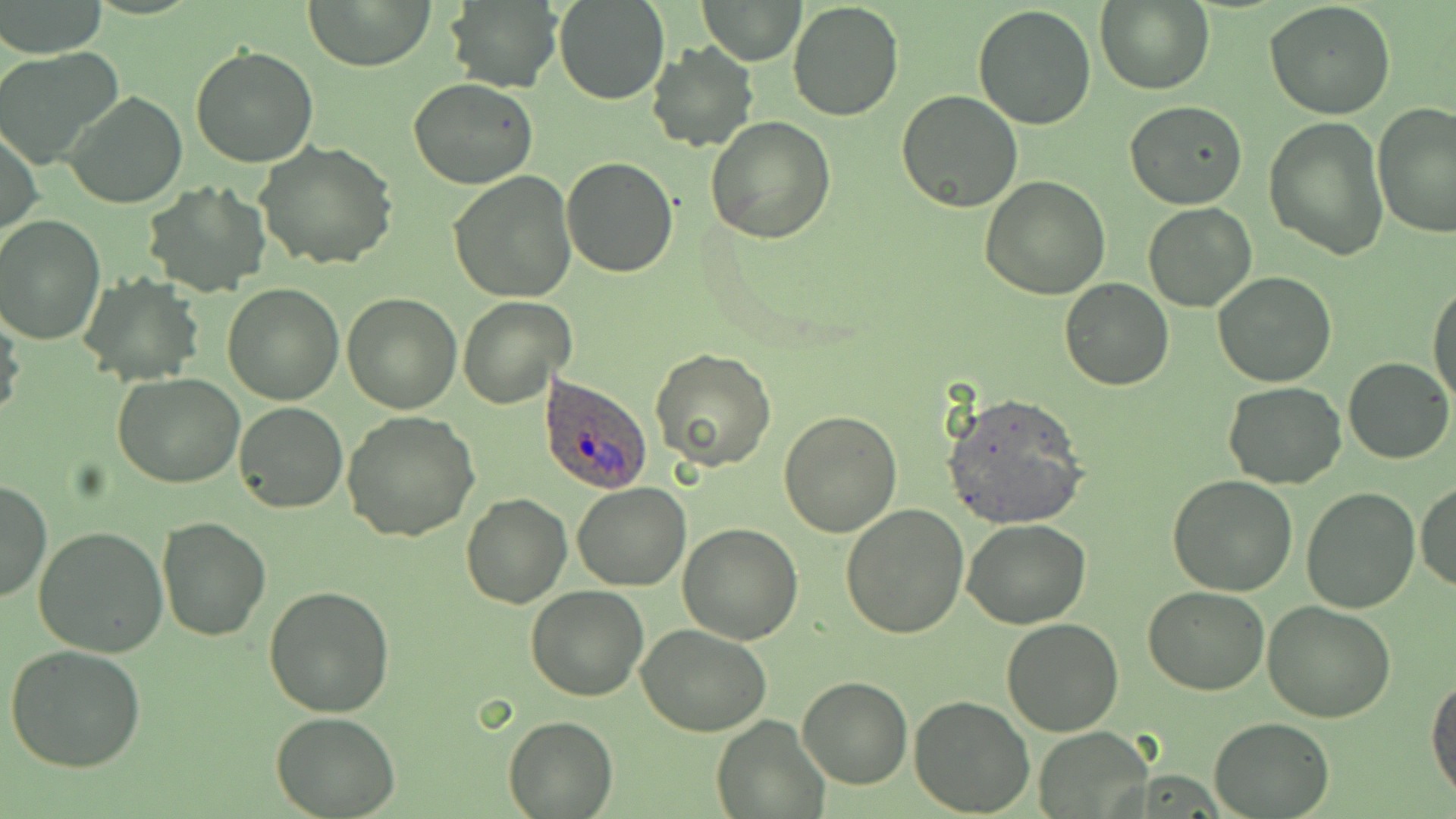

slide_level_diagnosis: Plasmodium ovale
modality: optical microscopy
uninfected_red_blood_cell_locations: 'approximate bounding boxes as (x1,y1)-(x2,y2) corner pairs in pixels: (306,0)-(434,71), (443,0)-(563,94), (787,0)-(904,119), (1096,0)-(1216,95), (3,1)-(109,56), (555,1)-(669,104), (698,1)-(805,64), (1265,2)-(1396,119), (973,4)-(1095,131), (646,43)-(759,152), (190,45)-(319,167), (0,47)-(123,167), (408,77)-(538,189), (896,89)-(1022,212), (64,91)-(186,209), (1123,101)-(1248,209), (1372,103)-(1455,237), (1265,116)-(1388,261), (706,117)-(836,243), (1,124)-(42,242), (256,141)-(398,269), (562,156)-(678,277), (448,172)-(577,302), (979,177)-(1112,299), (144,182)-(268,296), (1142,203)-(1257,312), (0,216)-(105,344), (1212,272)-(1338,388), (79,275)-(204,385), (1059,277)-(1174,391), (1428,279)-(1455,406), (223,284)-(344,405), (341,292)-(462,413), (458,295)-(575,409), (0,307)-(26,430), (651,348)-(776,472), (1344,357)-(1453,464), (112,373)-(246,489), (1224,381)-(1345,488), (941,392)-(1089,530), (232,402)-(347,514), (342,410)-(479,541), (778,410)-(904,537), (1167,473)-(1297,594), (0,480)-(50,604), (1414,480)-(1456,592), (571,482)-(690,590), (1300,486)-(1420,613), (461,492)-(571,609), (840,503)-(969,639), (155,517)-(271,641), (962,519)-(1092,628), (678,523)-(802,644), (32,525)-(168,659), (526,584)-(649,700), (1142,584)-(1271,695), (263,586)-(396,717), (1263,599)-(1396,721), (1002,617)-(1124,736), (638,623)-(770,736), (4,644)-(150,773), (1427,674)-(1456,803), (797,676)-(913,789), (908,695)-(1035,816), (272,710)-(400,818), (711,713)-(830,819), (503,715)-(617,818), (1208,716)-(1332,817), (1030,725)-(1155,818)'
magnification: 1000x
preparation: thin blood film
image_size: 1456×819 pixels
stain: May-Grünwald-Giemsa
field_of_view: one of a larger specimen
plasmodium_ovale_infected_red_blood_cell_locations: 'approximate bounding boxes as (x1,y1)-(x2,y2) corner pairs in pixels: (540,374)-(653,493)'